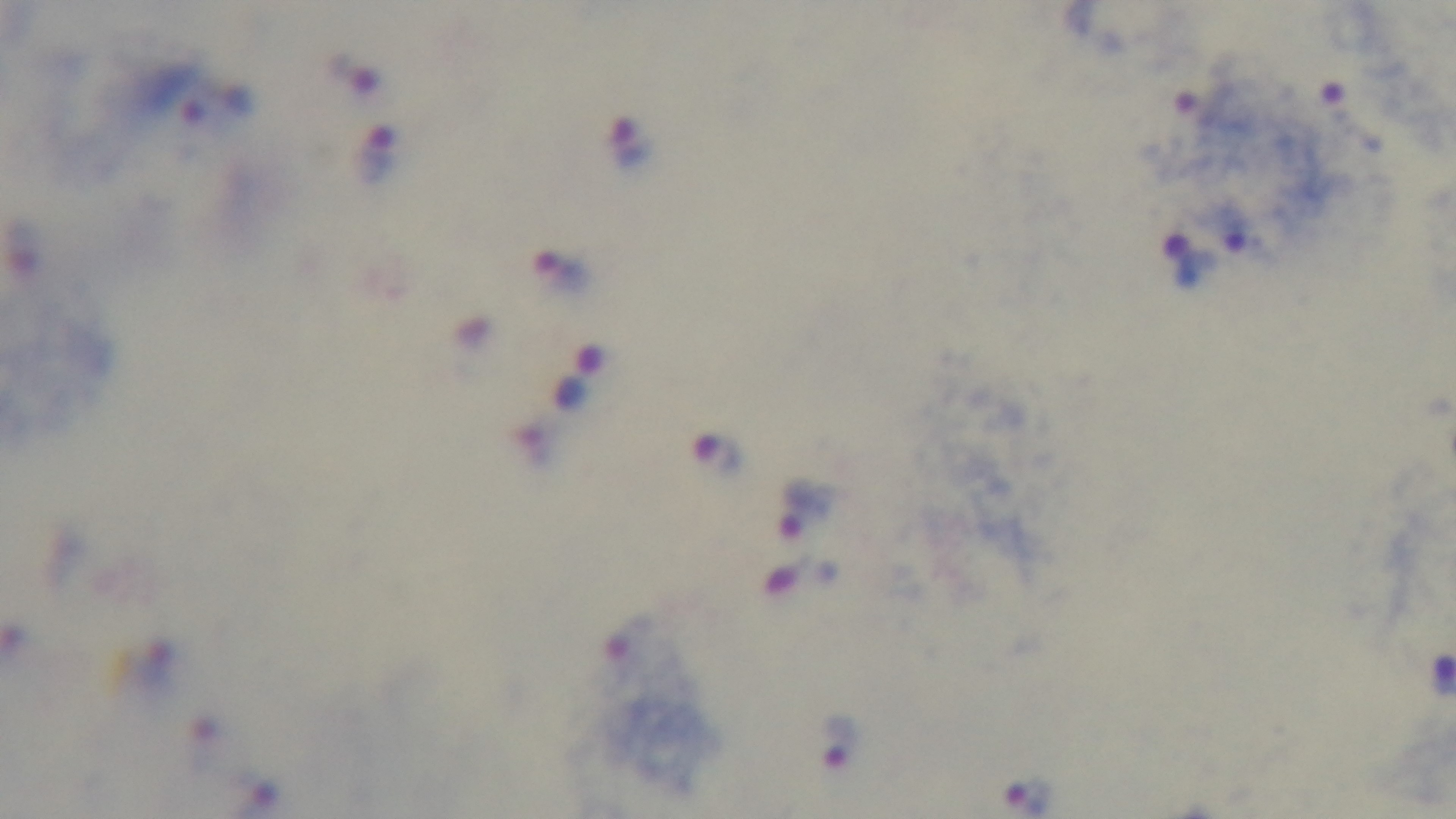

Summary:
  - Stain: Giemsa
  - Capture: mounted 4K digital camera
  - Malaria status: infected
  - Field of view: one from the slide
  - Modality: light microscopy
  - Preparation: thick
  - Objective: 100x oil immersion